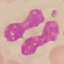
malaria status = uninfected
preparation = thin blood film
image type = automatically extracted cell patch, resized to 64 × 64 pixels
stain = Giemsa
capture = smartphone through the microscope eyepiece